State which parasite is depicted.
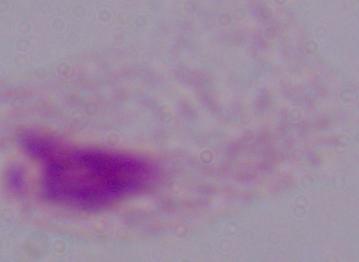

A trichomonad.

magnification = 1000x
modality = micrograph